Give the preparation type.
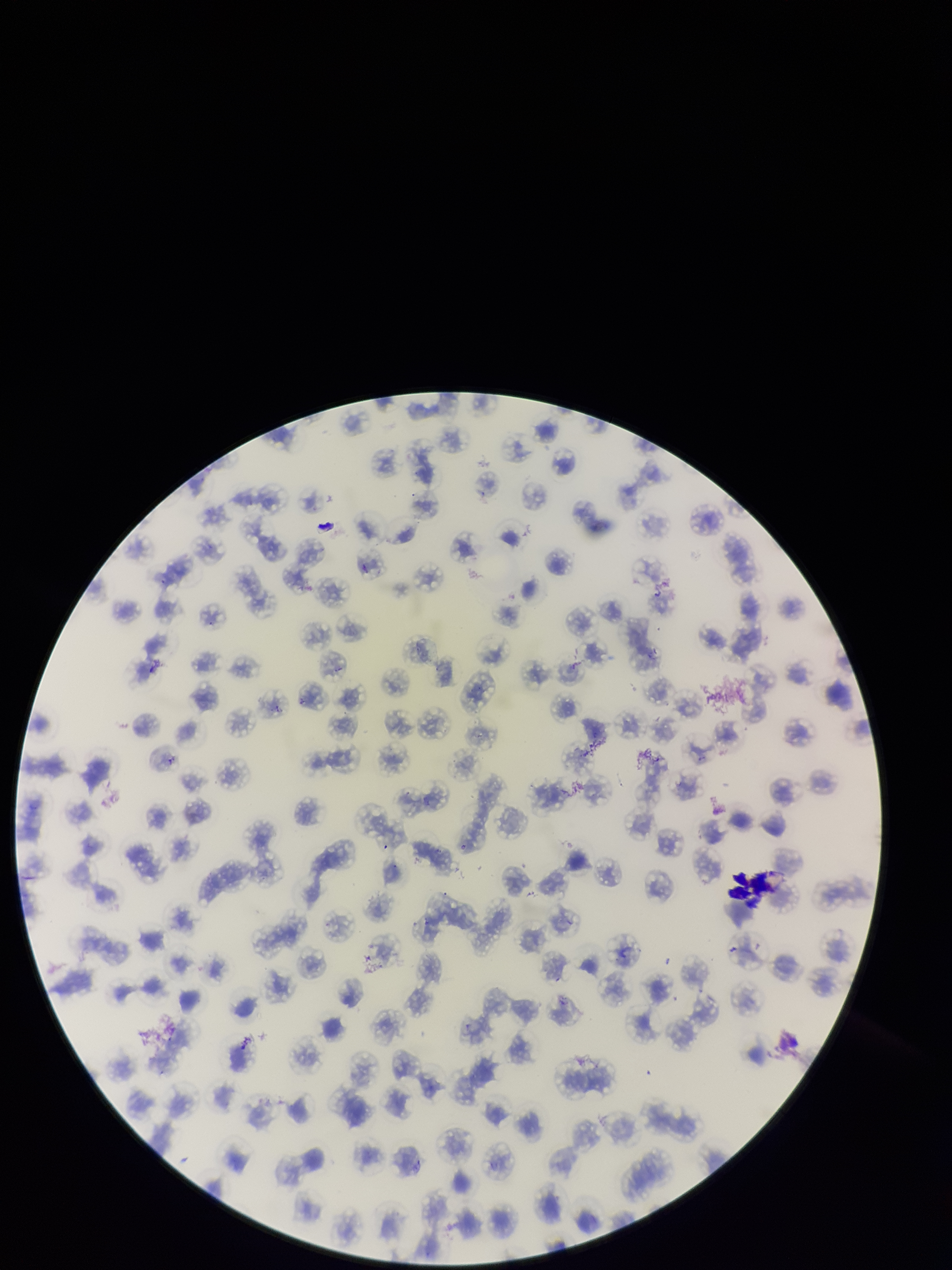
Thin.

parasitized red blood cell count = 0
field of view = single
patient malaria status = positive
species reported for this patient = Plasmodium falciparum
red blood cell count = 153
stain = Giemsa
parasitized red blood cells = none detected
image size = 952×1270 pixels
capture = smartphone photograph through the microscope eyepiece